Report the malaria status of this cell.
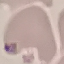
Uninfected.

capture = smartphone through the microscope eyepiece
image type = cell patch, automatically extracted from a larger field of view and resized to 64 × 64 pixels
stain = Giemsa
preparation = thin blood film